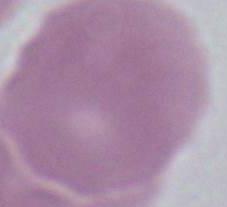

identification = erythrocyte
magnification = 1000x
modality = photomicrograph